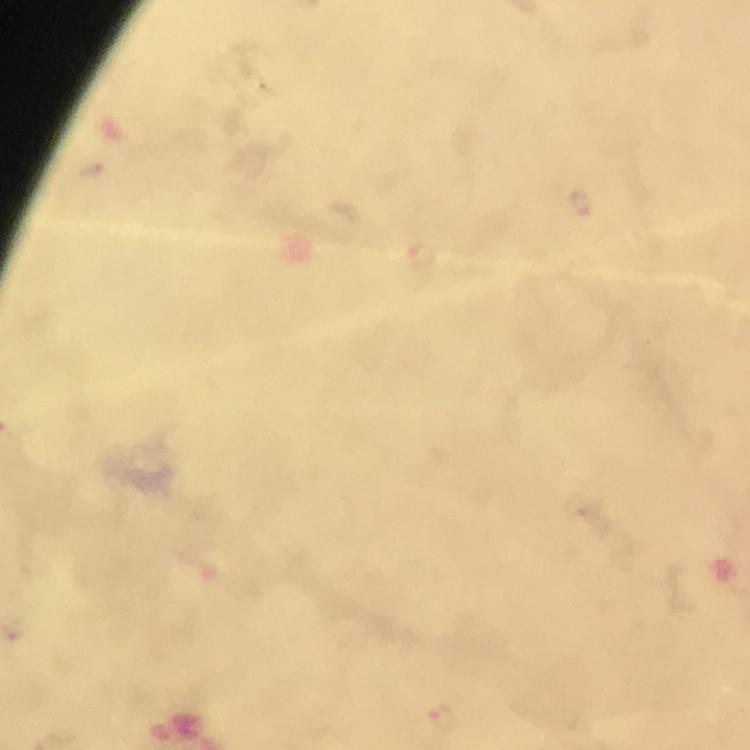

Approximate centers as {x, y} in pixels.
Summary:
  - Malaria parasite locations: {443, 720}
  - Capture: smartphone camera through the microscope
  - Cropped from: one field of view
  - Preparation: thick blood smear
  - Stain: Giemsa
  - Context: from a diagnostic examination for malaria
  - Image size: 750×750 pixels
  - Magnification: 100x
  - Immersion oil: applied